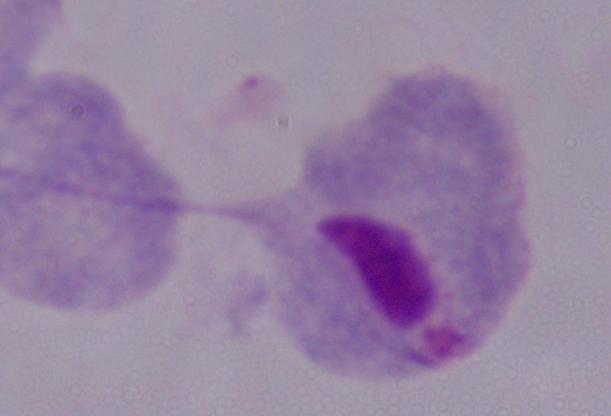
Summary:
  - Magnification: 1000x
  - Modality: photomicrograph
  - Identification: trichomonad